Give the extent of all Trypanosoma brucei.
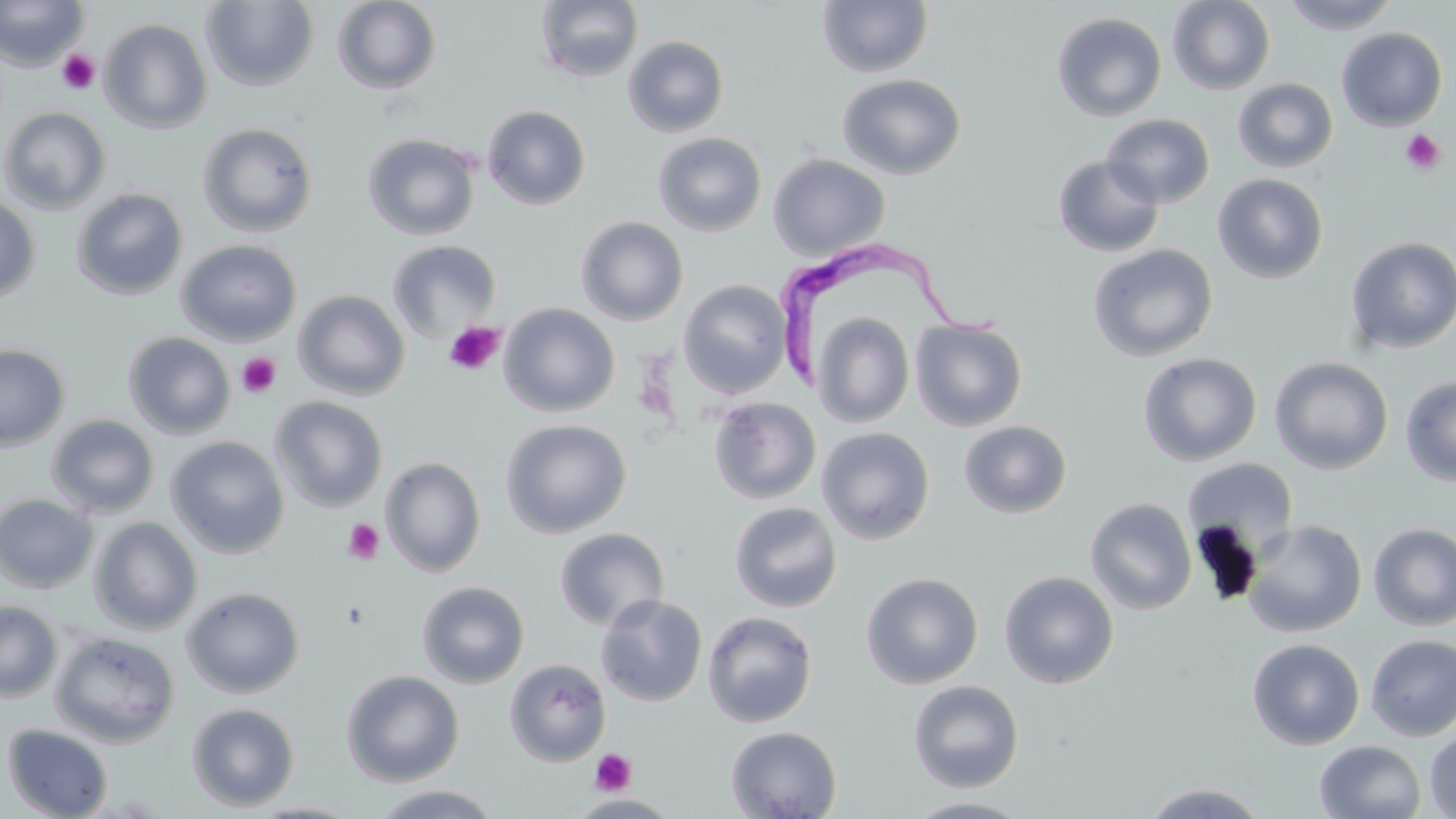
Approximate bounding boxes as (x1,y1)-(x2,y2) corner pairs in pixels.
Trypanosoma brucei: (776,237)-(1011,387).

slide_level_diagnosis: Trypanosoma brucei
image_size: 1456×819 pixels
preparation: thin blood smear
magnification: 1000x
uninfected_red_blood_cell_locations: 'approximate bounding boxes as (x1,y1)-(x2,y2) corner pairs in pixels: (0,0)-(89,71), (1167,0)-(1276,95), (1280,0)-(1402,35), (201,1)-(320,92), (331,1)-(442,95), (534,1)-(643,83), (817,1)-(933,78), (1051,12)-(1167,121), (99,18)-(213,134), (1336,27)-(1447,131), (622,35)-(729,137), (836,73)-(967,180), (1232,78)-(1339,173), (482,105)-(591,210), (0,106)-(112,214), (1102,113)-(1215,208), (197,122)-(319,237), (362,132)-(481,240), (652,132)-(767,237), (768,154)-(891,260), (1052,155)-(1165,257), (1212,174)-(1328,284), (71,187)-(188,301), (0,194)-(41,304), (576,216)-(689,325), (1345,236)-(1456,354), (176,239)-(301,346), (387,239)-(502,341), (1087,243)-(1218,362), (678,279)-(792,399), (293,290)-(411,400), (499,303)-(620,417), (811,311)-(915,428), (910,318)-(1028,431), (123,332)-(236,439), (0,343)-(70,453), (1138,352)-(1262,466), (1269,356)-(1394,475), (1400,375)-(1456,486), (269,395)-(388,512), (708,397)-(822,504), (716,397)-(831,610), (46,414)-(160,518), (500,418)-(631,538), (958,420)-(1072,518), (817,426)-(935,545), (165,436)-(289,558), (380,457)-(486,577), (1182,457)-(1299,560), (0,493)-(99,592), (1085,498)-(1197,615), (729,502)-(842,613), (89,516)-(203,635), (1243,519)-(1367,637), (1368,523)-(1456,631), (553,527)-(670,631), (999,571)-(1119,689), (861,572)-(984,689), (416,581)-(530,689), (181,585)-(306,698), (595,594)-(708,707), (0,600)-(62,701), (702,611)-(818,727), (50,631)-(181,747), (1365,633)-(1456,741), (1246,638)-(1365,750), (504,658)-(611,766), (341,669)-(465,786), (907,679)-(1024,792), (187,702)-(300,811), (1,724)-(114,818), (726,725)-(843,819), (1424,727)-(1456,818), (1313,740)-(1426,819), (1140,781)-(1272,818), (366,784)-(508,818), (902,796)-(1039,818)'
platelet_locations: 'approximate bounding boxes as (x1,y1)-(x2,y2) corner pairs in pixels: (56,49)-(99,95), (1400,130)-(1445,175), (443,321)-(505,376), (237,352)-(282,399), (342,518)-(385,565), (590,749)-(636,796)'
modality: light microscopy
stain: May-Grünwald-Giemsa
field_of_view: one of a larger specimen